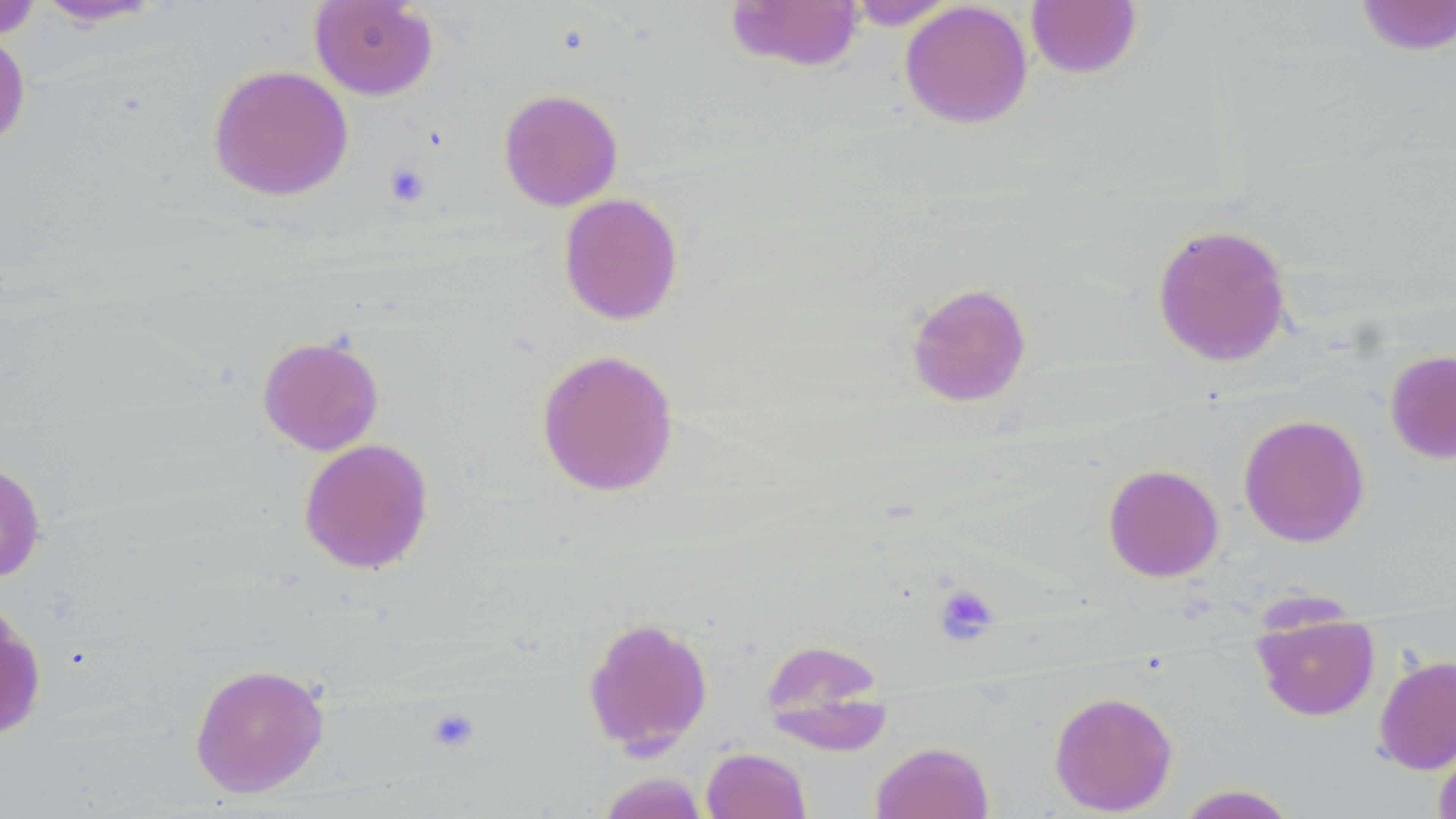
slide_level_diagnosis: no evidence of blood parasites
magnification: 1000x
stain: May-Grünwald-Giemsa
platelet_locations: 'approximate bounding boxes as (x1, y1, x2, y2) in pixels: (385, 162, 431, 207), (935, 584, 999, 644), (426, 707, 481, 755)'
preparation: thin blood film
image_size: 1456×819 pixels
modality: optical microscopy
uninfected_red_blood_cell_locations: 'approximate bounding boxes as (x1, y1, x2, y2) in pixels: (31, 0, 169, 28), (308, 0, 439, 100), (723, 0, 865, 73), (1353, 0, 1456, 57), (0, 1, 45, 40), (842, 1, 960, 29), (899, 1, 1033, 129), (1025, 1, 1143, 79), (0, 29, 31, 152), (207, 64, 353, 201), (497, 88, 623, 211), (558, 193, 684, 325), (1151, 222, 1294, 367), (905, 281, 1032, 407), (257, 334, 384, 456), (535, 348, 679, 497), (1385, 350, 1456, 464), (1238, 413, 1370, 547), (298, 437, 434, 575), (0, 459, 47, 584), (1102, 463, 1224, 582), (0, 596, 48, 742), (1252, 610, 1380, 722), (582, 615, 713, 756), (759, 638, 891, 752), (1373, 654, 1456, 775), (189, 662, 330, 798), (1048, 691, 1178, 815), (1433, 732, 1456, 819), (870, 741, 994, 819), (701, 747, 812, 819), (595, 772, 710, 819), (1175, 784, 1301, 818)'
field_of_view: one of a larger specimen